Identify the cell.
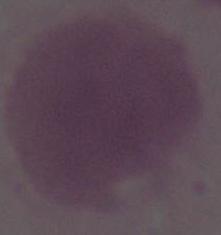
This is an erythrocyte.

Micrograph. Captured at 1000x magnification.